Report the malaria status of this cell.
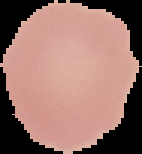

It is uninfected.

Image is 142×154 pixels. From a thin blood smear. Cell region segmented out of the field of view; the surrounding area is masked to black.